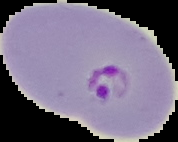
Summary:
  - Result: Plasmodium parasites detected
  - Image type: cell region segmented out of the field of view; surrounding area masked to black
  - Image size: 178×142 pixels
  - Preparation: thin blood film